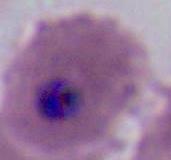 Micrograph. 400x or 1000x magnification. A Plasmodium parasite is shown.